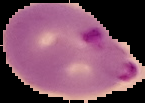

Summary:
  - Result: Plasmodium parasites identified
  - Image type: segmented cell region with the area outside set to black
  - Image size: 145×103 pixels
  - Preparation: thin blood smear